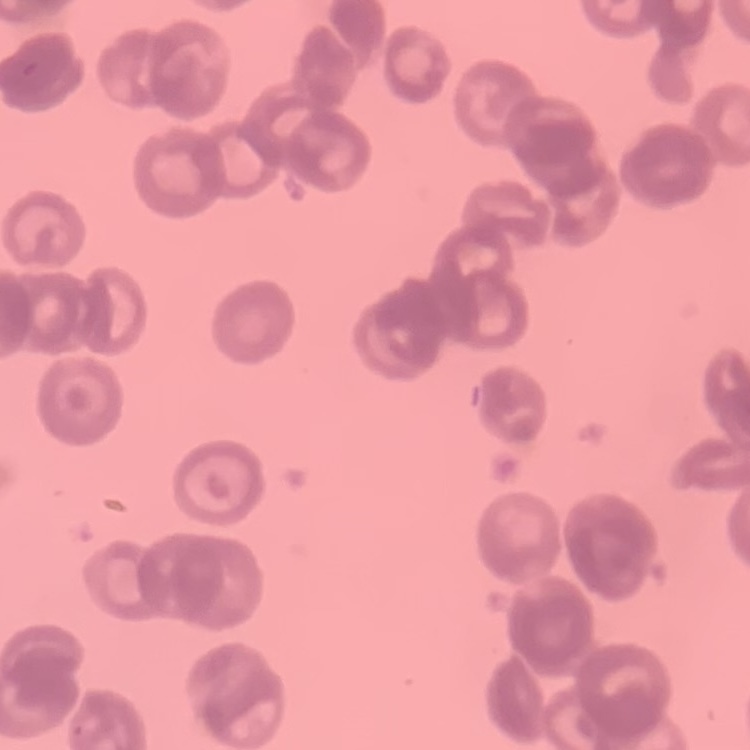
Summary:
  - Erythrocyte morphology: rouleaux formation
  - Stain: Field's or Giemsa
  - Image type: one tile cut from a larger photomicrograph
  - Preparation: thin peripheral smear